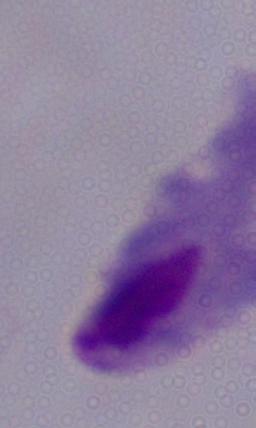

Photomicrograph. A trichomonad is shown. 1000x magnification.